Give the position of every leukocyte visible.
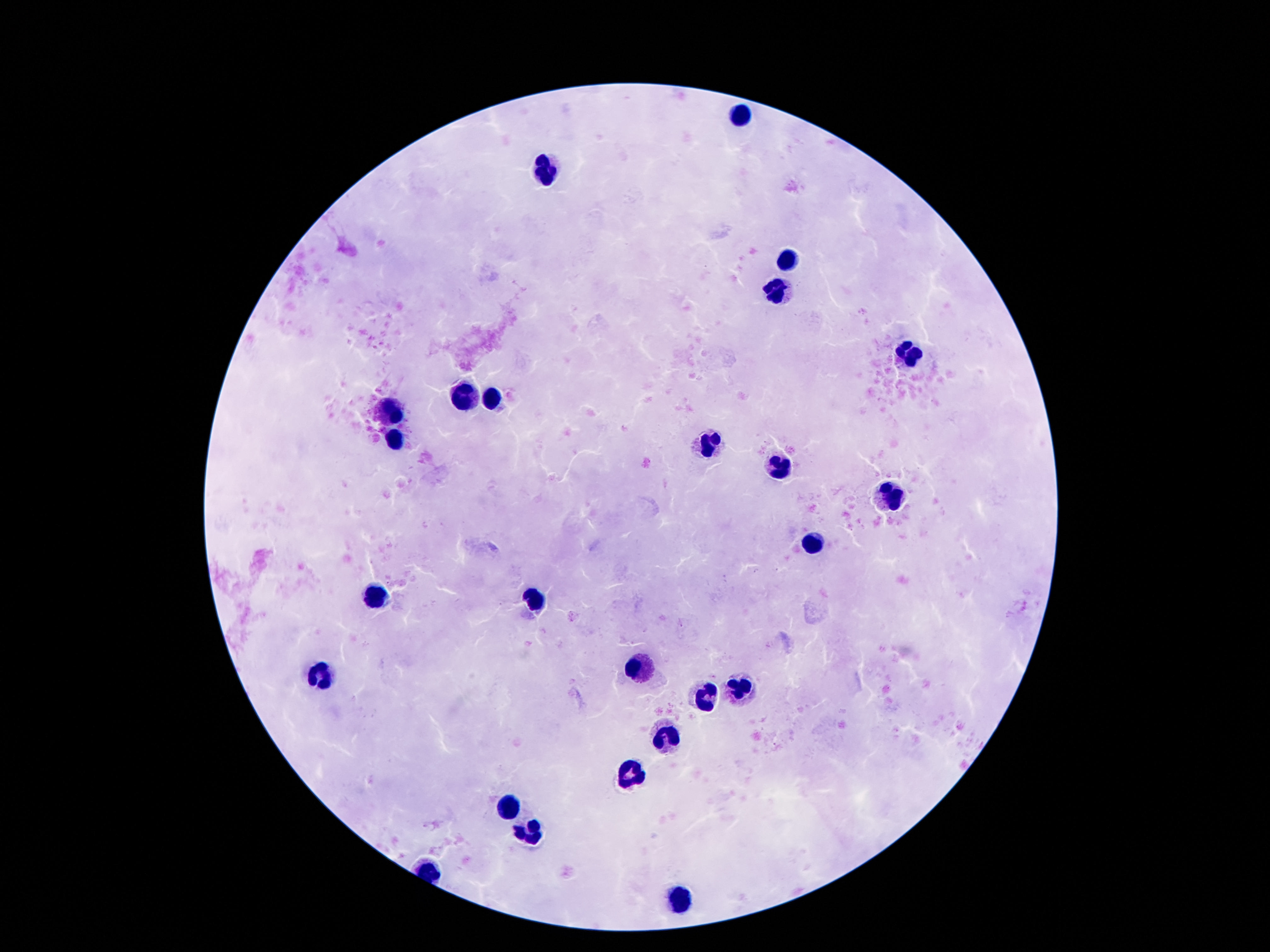
Approximate centers as [x, y] in pixels.
Leukocytes: [739, 113], [546, 171], [787, 261], [774, 295], [914, 353], [465, 398], [492, 400], [392, 414], [394, 441], [708, 441], [778, 466], [894, 497], [812, 544], [376, 594], [533, 596], [639, 667], [324, 675], [739, 687], [706, 700], [667, 739], [631, 774], [508, 807], [530, 834], [681, 900].

One field from this slide. Image is 1270×952 pixels. Thick peripheral-blood smear. 100x magnification. Patient malaria status: negative. Smartphone photograph taken through the microscope eyepiece. Giemsa-stained preparation.